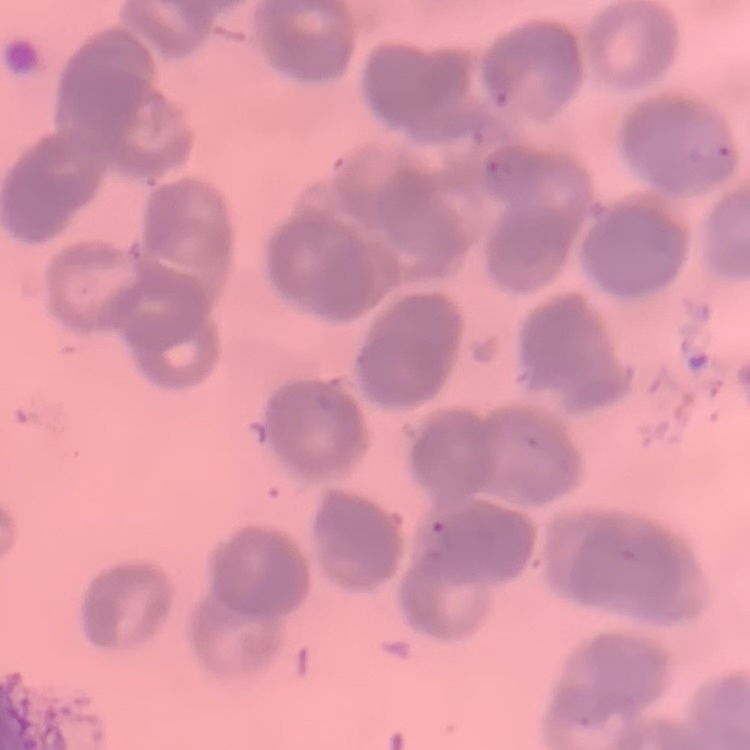 The red blood cells exhibit rouleaux formation. Thin blood film. Field's or Giemsa stain. One tile cut from a larger photomicrograph.